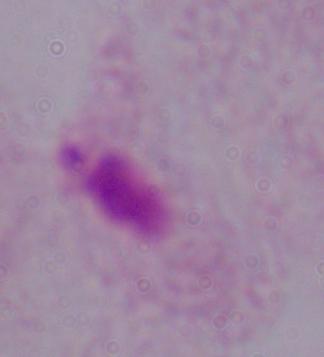

magnification: 1000x
modality: micrograph
identification: trichomonad